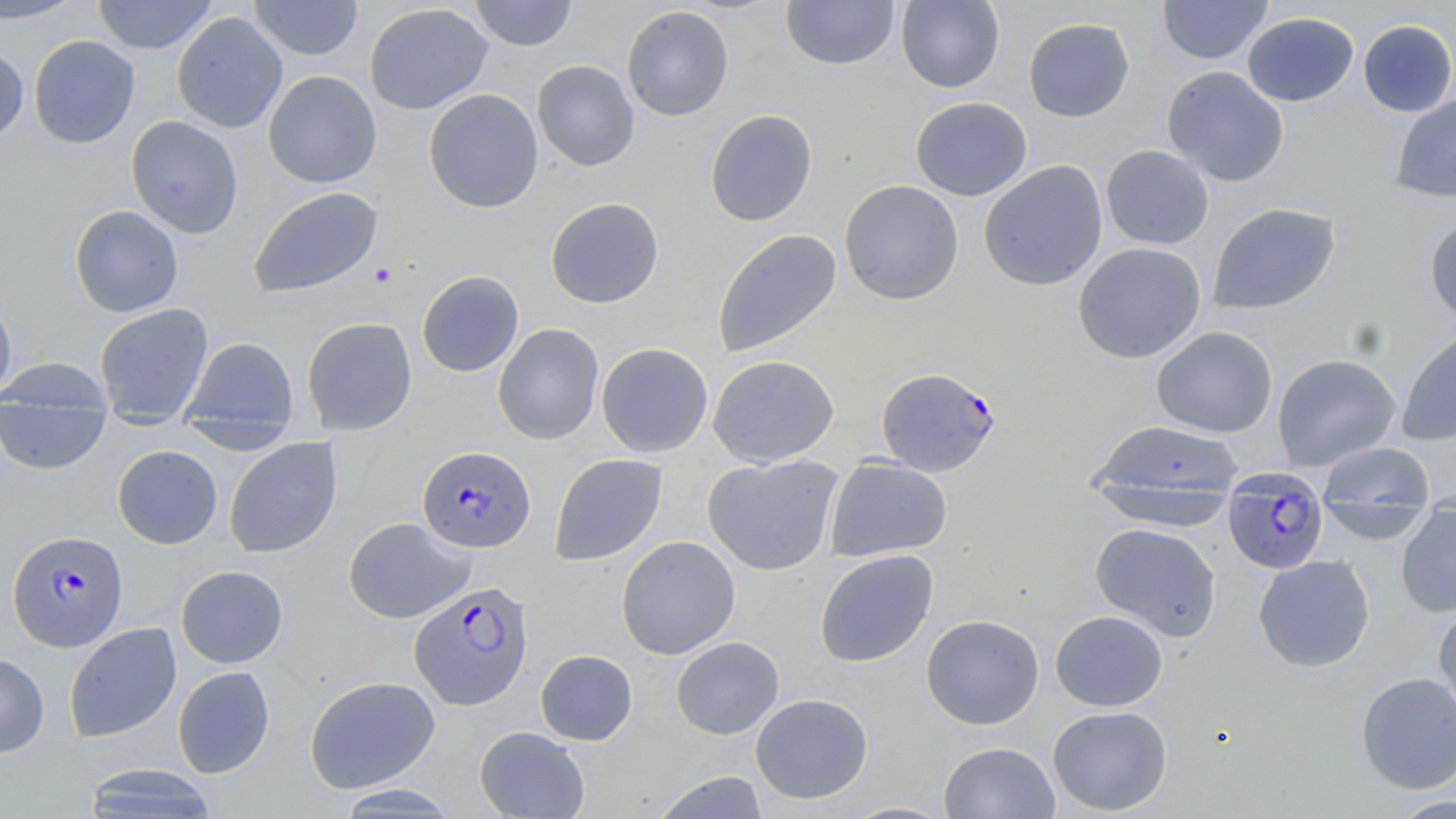
Approximate bounding boxes as (x1, y1, x2, y2) in pixels. Uninfected red blood cell locations: (0, 0, 87, 24), (93, 0, 217, 55), (248, 0, 363, 61), (469, 0, 577, 51), (780, 0, 900, 70), (895, 0, 1005, 92), (1157, 0, 1273, 64), (364, 3, 493, 115), (621, 5, 734, 121), (172, 11, 288, 133), (1242, 12, 1359, 106), (1023, 17, 1135, 122), (1358, 19, 1456, 116), (28, 35, 140, 149), (0, 45, 29, 145), (532, 59, 640, 171), (1161, 66, 1289, 187), (262, 70, 382, 188), (424, 88, 543, 213), (1389, 94, 1456, 203), (910, 96, 1032, 201), (705, 109, 818, 227), (126, 115, 244, 239), (1101, 145, 1214, 250), (979, 160, 1108, 291), (839, 180, 964, 305), (247, 186, 383, 298), (545, 197, 664, 309), (1207, 202, 1340, 315), (69, 204, 184, 318), (1424, 215, 1456, 327), (711, 229, 842, 358), (1072, 242, 1207, 363), (416, 270, 524, 377), (0, 291, 17, 404), (94, 303, 214, 417), (301, 317, 417, 435), (492, 323, 604, 445), (1396, 325, 1456, 447), (1151, 326, 1278, 438), (182, 336, 298, 430), (596, 342, 714, 458), (1271, 353, 1401, 470), (707, 354, 839, 468), (0, 358, 115, 414), (0, 402, 112, 475), (178, 418, 300, 454), (1088, 420, 1246, 508), (224, 437, 342, 559), (1316, 440, 1436, 530), (112, 445, 223, 549), (549, 453, 668, 566), (702, 453, 844, 576), (825, 457, 952, 562), (1088, 482, 1241, 531), (1395, 506, 1456, 618), (343, 517, 475, 623), (1089, 523, 1223, 642), (616, 535, 741, 660), (814, 549, 939, 667), (1253, 554, 1376, 672), (175, 565, 288, 668), (1433, 603, 1456, 727), (1050, 610, 1168, 711), (921, 613, 1045, 730), (64, 622, 181, 742), (671, 636, 784, 740), (535, 649, 638, 745), (0, 653, 49, 758), (172, 666, 275, 778), (1356, 671, 1456, 794), (304, 675, 440, 793), (750, 693, 873, 804), (1048, 705, 1172, 816), (473, 726, 590, 818), (938, 742, 1060, 818), (81, 763, 220, 818), (650, 771, 770, 819), (333, 784, 462, 816), (1385, 795, 1456, 819), (838, 801, 956, 818). Plasmodium falciparum-infected red blood cell locations: (875, 366, 1001, 477), (417, 445, 536, 553), (1223, 479, 1328, 575), (7, 529, 129, 652), (409, 581, 533, 710). Slide-level diagnosis: Plasmodium falciparum. Thin blood film. 1000x magnification. Light microscopy. One field of a larger specimen. Image is 1456×819 pixels. May-Grünwald-Giemsa stain.